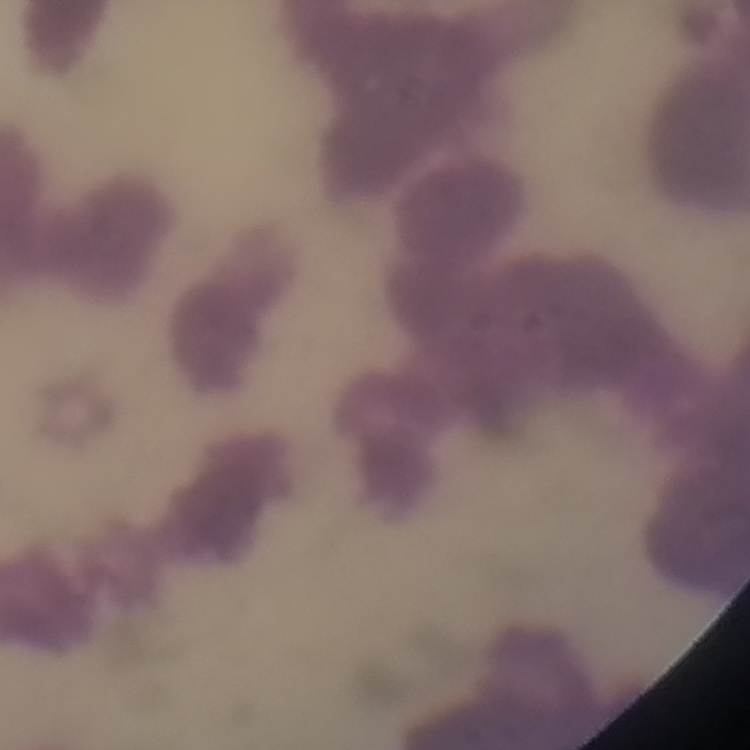
Summary:
  - Red blood cell morphology: rouleaux formation
  - Image type: one tile cut from a larger photomicrograph
  - Stain: Field's or Giemsa
  - Preparation: thin blood smear